State which parasite is depicted.
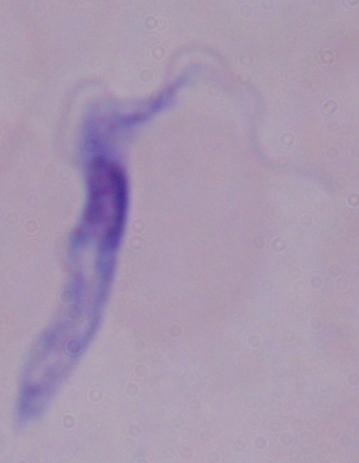
A trypanosome.

1000x magnification. Photomicrograph.